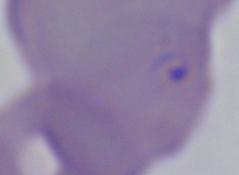

identification = Babesia
magnification = 1000x
modality = photomicrograph